Point out Plasmodium parasites and leukocytes.
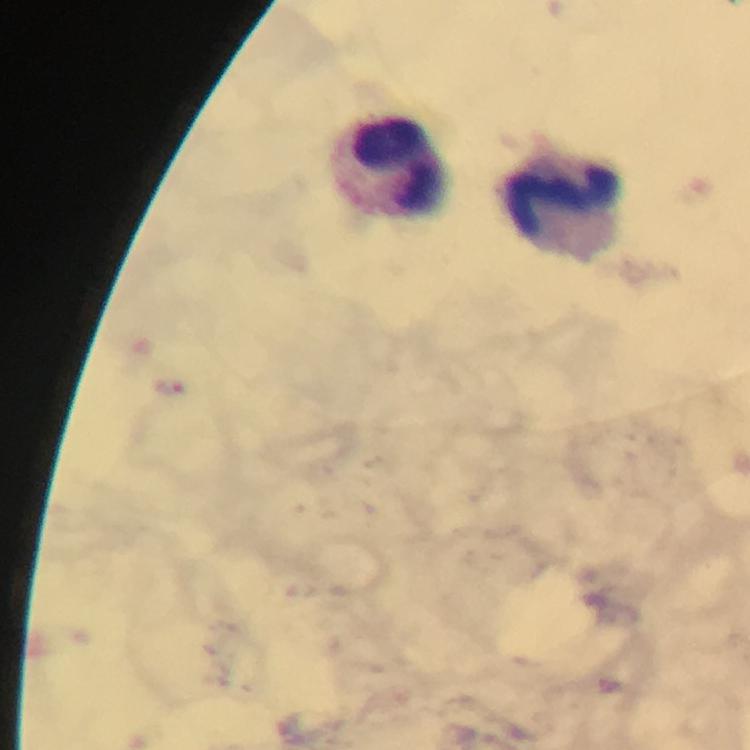
Approximate object centers, in pixels from the top-left corner.
Plasmodium parasites: (x=169, y=385).
Leukocytes: (x=394, y=168), (x=567, y=213).

image_size: 750×750 pixels
cropped_from: one field of view
immersion_oil: used
preparation: thick smear
capture: smartphone photograph through a microscope
magnification: 100x
context: from a malaria diagnostic workup
stain: Giemsa